Name the parasite shown.
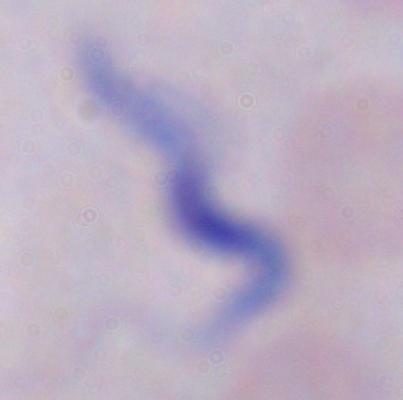

This is a trypanosome.

Photomicrograph. Captured at 1000x magnification.